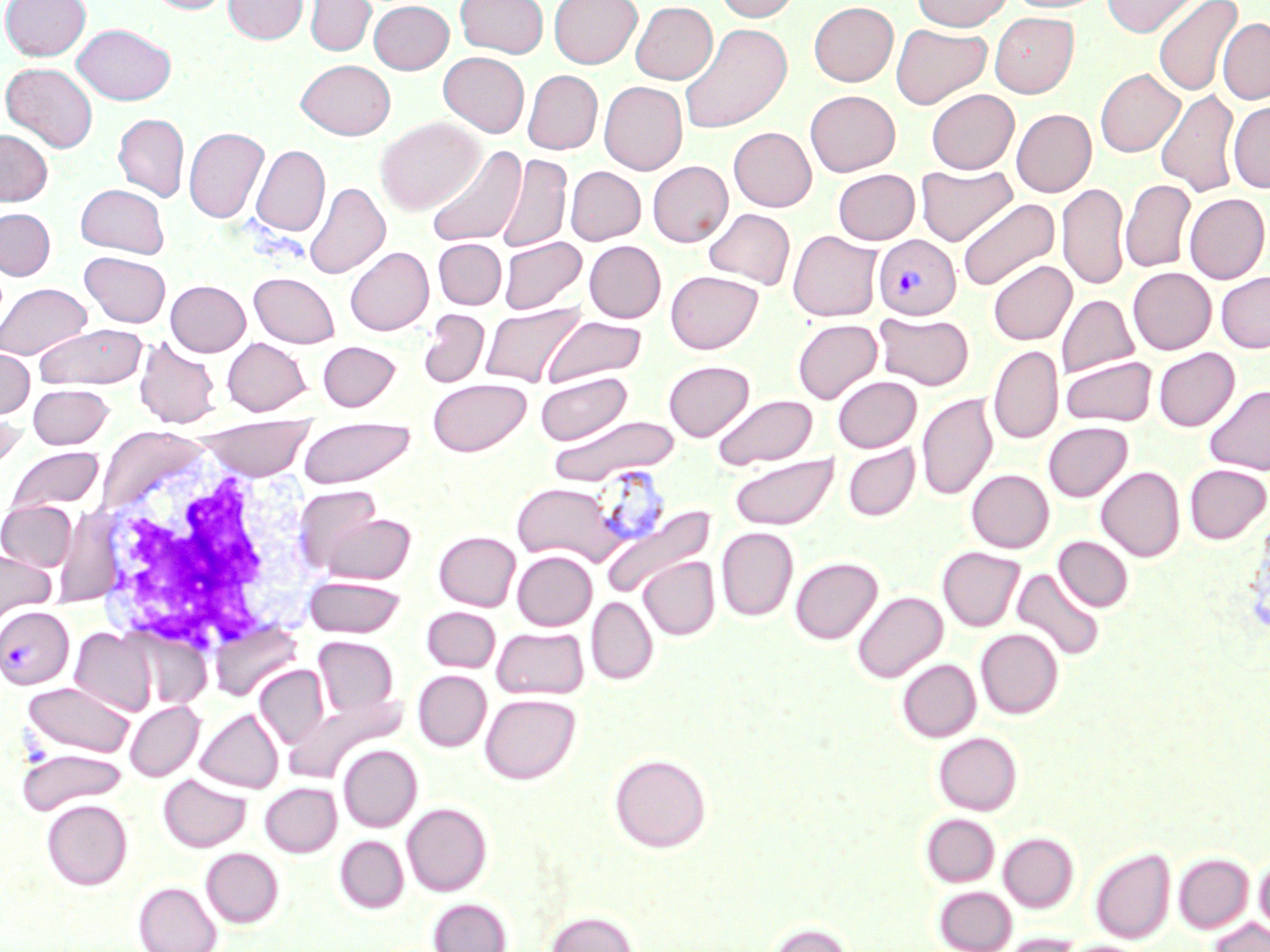

slide-level diagnosis = Plasmodium vivax
stain = May-Grünwald-Giemsa
magnification = 1000x
modality = optical microscopy
field of view = single
white blood cell locations = approximate bounding boxes as [x1, y1, x2, y2] in pixels: [89, 445, 320, 660]
preparation = thin blood film
uninfected red blood cell locations = approximate bounding boxes as [x1, y1, x2, y2] in pixels: [1, 0, 91, 60], [146, 0, 233, 14], [223, 0, 308, 44], [305, 0, 376, 56], [455, 0, 548, 58], [549, 0, 642, 68], [714, 0, 801, 22], [912, 0, 1011, 31], [1007, 0, 1105, 13], [1102, 0, 1203, 37], [1153, 0, 1243, 96], [369, 1, 453, 74], [631, 1, 717, 84], [809, 1, 899, 86], [990, 12, 1079, 97], [1218, 18, 1270, 104], [72, 23, 176, 105], [679, 23, 792, 133], [890, 24, 991, 109], [439, 52, 529, 137], [296, 59, 396, 139], [1, 62, 98, 152], [1095, 68, 1184, 157], [523, 70, 603, 154], [599, 81, 687, 175], [926, 89, 1019, 173], [1155, 89, 1241, 196], [805, 90, 900, 176], [1228, 102, 1270, 193], [1011, 109, 1096, 197], [113, 114, 189, 201], [375, 117, 484, 215], [184, 127, 269, 224], [728, 127, 817, 211], [0, 129, 52, 205], [251, 145, 330, 236], [425, 145, 527, 248], [496, 153, 571, 253], [647, 161, 733, 247], [916, 163, 1017, 246], [565, 166, 646, 245], [833, 168, 920, 244], [1120, 179, 1196, 273], [304, 181, 390, 279], [1058, 182, 1129, 290], [75, 183, 170, 258], [1184, 193, 1269, 283], [957, 197, 1060, 291], [0, 207, 55, 280], [704, 208, 795, 289], [788, 230, 883, 321], [498, 236, 587, 314], [433, 238, 507, 309], [584, 240, 665, 323], [345, 246, 434, 335], [80, 252, 171, 327], [988, 260, 1077, 345], [1128, 267, 1216, 354], [665, 270, 763, 353], [1216, 271, 1270, 352], [249, 272, 340, 348], [166, 280, 250, 356], [0, 282, 91, 360], [1057, 295, 1139, 378], [480, 302, 587, 387], [418, 309, 489, 388], [874, 313, 974, 390], [542, 315, 647, 386], [792, 319, 882, 403], [34, 324, 148, 389], [134, 336, 222, 428], [222, 337, 311, 415], [318, 341, 400, 410], [988, 345, 1063, 444], [0, 348, 34, 418], [1153, 348, 1240, 431], [1060, 356, 1157, 427], [663, 360, 754, 441], [535, 372, 633, 445], [833, 376, 921, 452], [427, 378, 531, 456], [27, 384, 114, 449], [1204, 385, 1270, 475], [917, 393, 997, 501], [712, 394, 818, 470], [0, 414, 27, 478], [548, 415, 680, 485], [193, 416, 316, 481], [297, 418, 416, 487], [1043, 421, 1132, 501], [843, 444, 920, 521], [6, 446, 103, 515], [729, 454, 839, 529], [1184, 464, 1269, 543], [1096, 466, 1185, 562], [966, 469, 1054, 553], [511, 482, 621, 565], [1, 500, 77, 571], [599, 503, 716, 600], [305, 505, 417, 585], [716, 527, 798, 620], [434, 530, 520, 610], [1053, 536, 1133, 612], [937, 546, 1024, 631], [0, 547, 56, 624], [512, 550, 597, 630], [639, 556, 720, 640], [790, 556, 883, 644], [1012, 568, 1105, 662], [305, 576, 404, 637], [852, 591, 947, 683], [586, 596, 658, 685], [421, 606, 501, 672], [492, 626, 589, 699], [70, 627, 158, 717], [976, 628, 1063, 718], [313, 636, 399, 720], [897, 659, 980, 742], [254, 665, 330, 750], [413, 670, 492, 751], [22, 681, 136, 759], [480, 693, 581, 784], [125, 701, 204, 781], [195, 707, 283, 793], [933, 732, 1022, 815], [338, 745, 422, 832], [17, 748, 127, 815], [608, 753, 712, 853], [158, 774, 251, 852], [260, 783, 342, 857], [42, 799, 132, 889], [402, 802, 492, 896], [920, 813, 1000, 887], [998, 832, 1078, 912], [335, 836, 408, 913], [1090, 847, 1175, 944], [201, 848, 283, 927], [1174, 853, 1254, 933], [1255, 854, 1270, 934], [134, 882, 221, 952], [933, 886, 1017, 952], [428, 898, 511, 951], [545, 910, 638, 952], [1208, 918, 1268, 952], [766, 921, 853, 952], [1000, 933, 1083, 952]
image size = 1270×952 pixels
Plasmodium vivax-infected red blood cell locations = approximate bounding boxes as [x1, y1, x2, y2] in pixels: [873, 234, 961, 319], [588, 464, 672, 553], [0, 605, 74, 689]